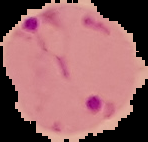
The area outside the segmented cell region is set to black. From a thin blood film. Image is 148×142 pixels. Malaria status: parasitized.